Assess the morphology of the red blood cells.
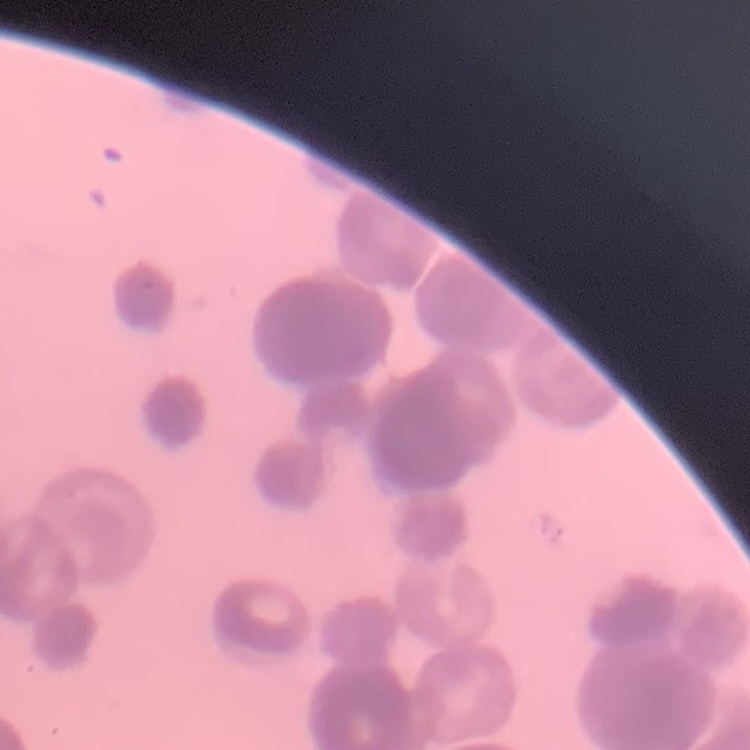
Rouleaux formation.

image_type: square crop of a larger photomicrograph
preparation: thin blood film
stain: Field's or Giemsa